Classify this cell by malaria status.
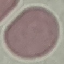

Uninfected.

capture = smartphone camera at the microscope eyepiece
image type = cell patch, automatically extracted from a larger field of view and resized to 64 × 64 pixels
stain = Giemsa
preparation = thin smear